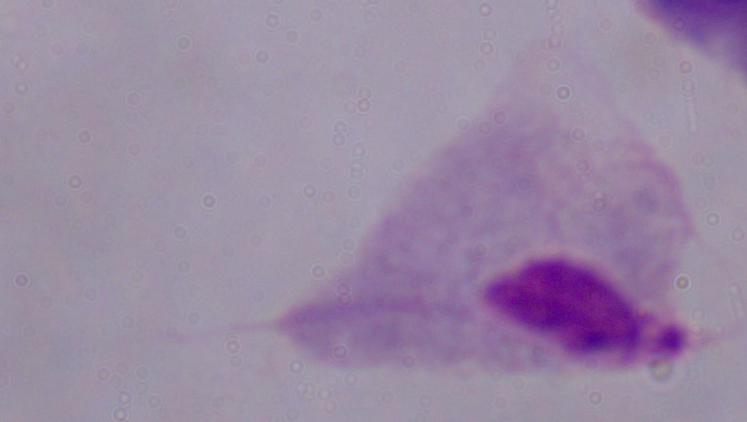
A trichomonad is shown. Captured at 1000x magnification. Photomicrograph.